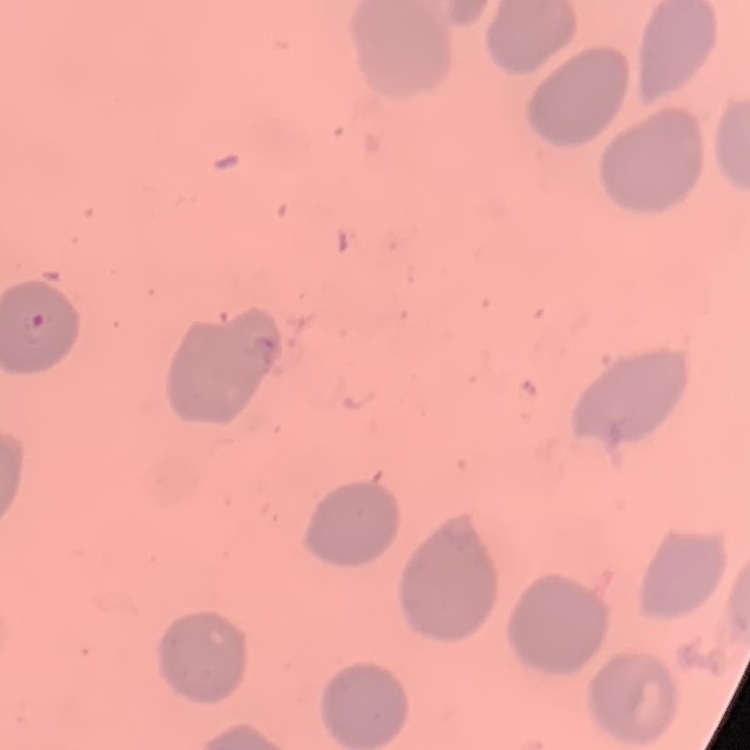
Summary:
  - Erythrocyte morphology: no rouleaux formation
  - Stain: Field's or Giemsa
  - Image type: one tile cut from a larger photomicrograph
  - Preparation: thin blood film